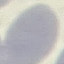

result = negative for malaria parasites
image type = automatically extracted cell patch, resized to 64 × 64 pixels
capture = smartphone through the microscope eyepiece
stain = Giemsa
preparation = thin smear